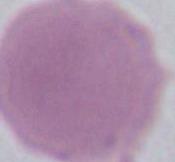

A red blood cell is shown. Captured at 1000x magnification. Photomicrograph.